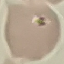

Summary:
  - Malaria status: uninfected
  - Image type: automatically extracted cell patch, resized to 64 × 64 pixels
  - Capture: smartphone camera at the microscope eyepiece
  - Preparation: thin smear
  - Stain: Giemsa